Name the parasite shown.
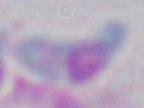

This is Toxoplasma gondii.

modality = micrograph
magnification = 1000x